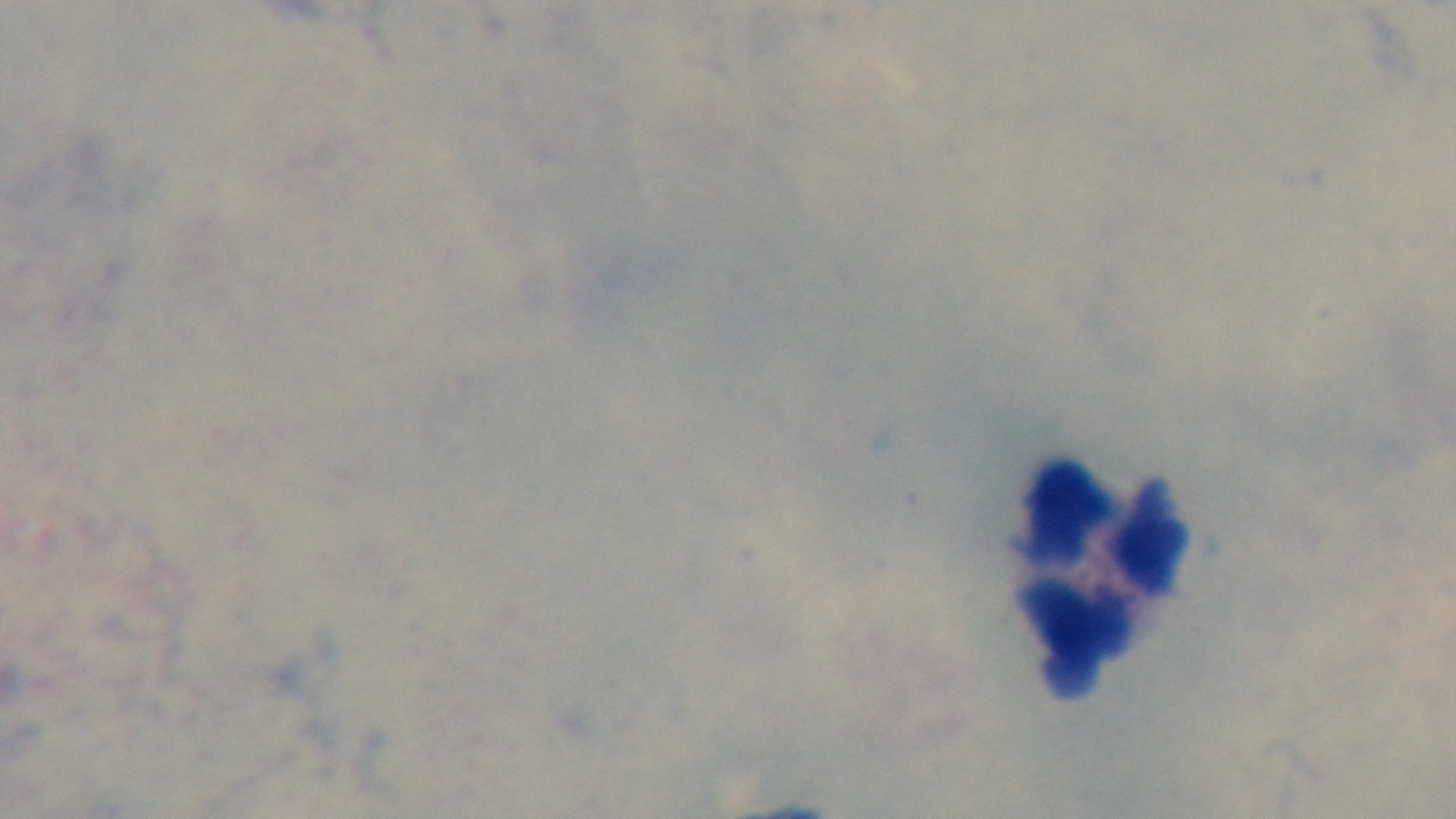

Summary:
  - Capture: mounted 4K digital camera
  - Objective: 100x oil immersion
  - Preparation: thick
  - Field of view: one from the slide
  - Modality: light microscopy
  - Malaria status: negative
  - Stain: Giemsa